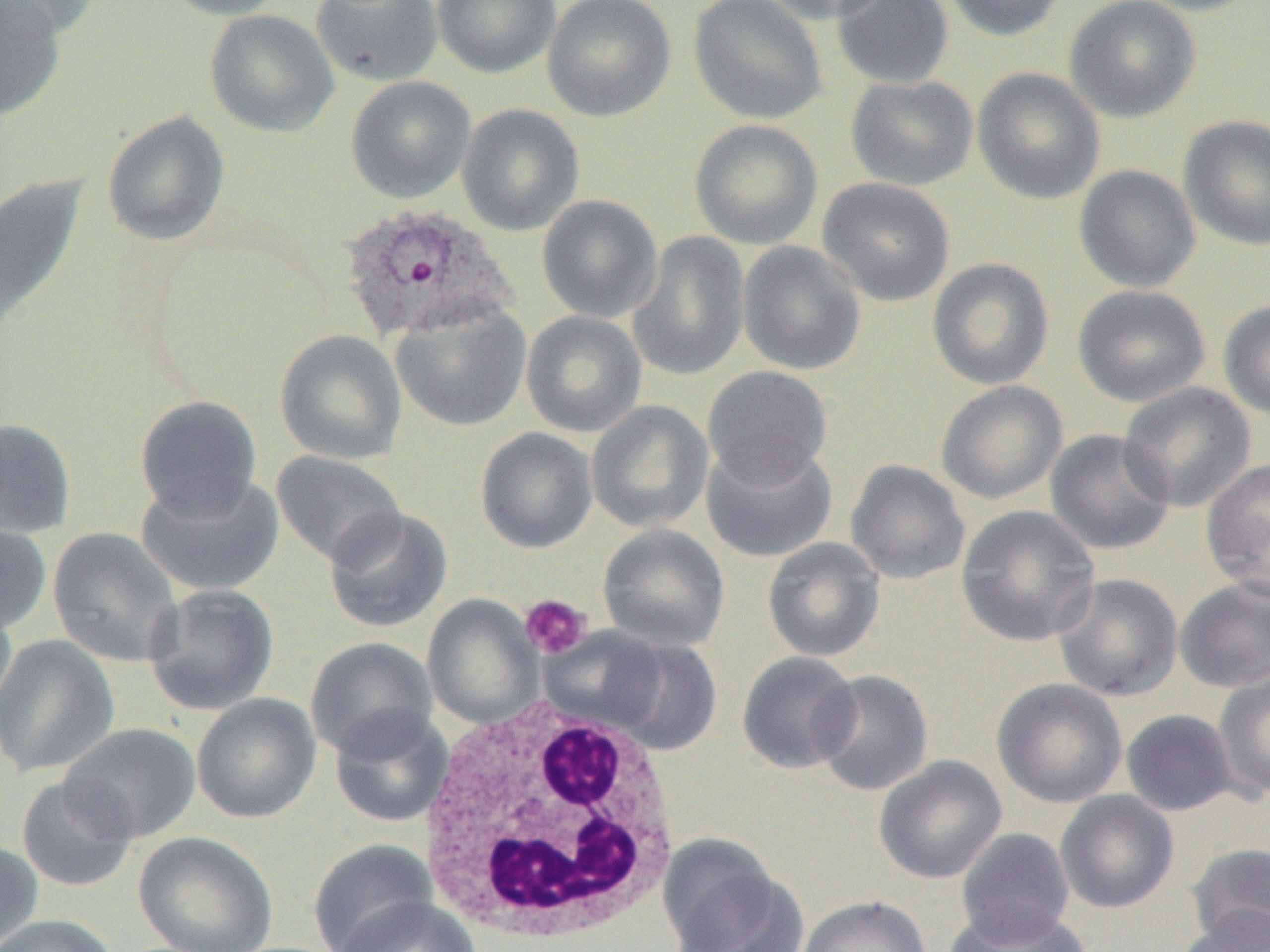

Approximate bounding boxes as [x1, y1, x2, y2] in pixels. White blood cell locations: [413, 698, 686, 945]. Plasmodium ovale-infected red blood cell locations: [339, 204, 516, 344]. Uninfected red blood cell locations: [0, 0, 103, 38], [0, 0, 66, 120], [156, 0, 293, 20], [311, 0, 444, 87], [431, 0, 561, 79], [542, 0, 676, 122], [688, 0, 829, 125], [759, 0, 895, 25], [832, 0, 954, 89], [939, 0, 1067, 41], [1064, 0, 1201, 123], [1130, 0, 1262, 16], [204, 9, 340, 137], [972, 67, 1106, 205], [345, 75, 476, 204], [845, 75, 978, 190], [456, 103, 585, 237], [101, 111, 231, 246], [1178, 114, 1270, 251], [689, 119, 823, 250], [1074, 164, 1202, 293], [0, 175, 88, 343], [817, 177, 956, 307], [536, 194, 663, 323], [627, 231, 750, 381], [737, 240, 867, 376], [927, 257, 1054, 390], [1072, 284, 1210, 407], [1218, 299, 1270, 420], [390, 301, 531, 432], [521, 311, 647, 438], [274, 330, 407, 465], [702, 366, 833, 487], [936, 380, 1068, 505], [1118, 382, 1257, 513], [134, 394, 263, 519], [586, 400, 714, 533], [0, 418, 77, 540], [474, 427, 598, 553], [1044, 429, 1176, 556], [701, 440, 838, 563], [270, 450, 407, 568], [1201, 457, 1270, 599], [845, 459, 970, 585], [136, 472, 284, 597], [956, 505, 1100, 647], [322, 506, 454, 635], [0, 520, 51, 635], [597, 524, 730, 652], [47, 528, 183, 667], [762, 537, 886, 662], [1052, 573, 1183, 702], [1174, 577, 1270, 693], [143, 584, 280, 716], [0, 593, 18, 720], [422, 594, 543, 728], [584, 631, 722, 756], [0, 634, 121, 777], [305, 637, 439, 760], [736, 651, 862, 774], [1214, 667, 1270, 800], [812, 669, 934, 796], [991, 678, 1127, 809], [191, 692, 322, 824], [328, 708, 453, 828], [1120, 708, 1240, 816], [59, 722, 202, 843], [874, 755, 1007, 884], [16, 775, 138, 892], [1055, 790, 1179, 913], [955, 827, 1075, 946], [133, 831, 278, 952], [0, 839, 43, 950], [307, 839, 438, 952], [658, 840, 802, 952], [1187, 842, 1270, 948], [796, 895, 931, 952], [336, 896, 483, 952], [945, 906, 1091, 952], [1179, 906, 1270, 952], [0, 914, 120, 952]. Platelet locations: [520, 594, 592, 660]. Slide-level diagnosis: Plasmodium ovale. Optical microscopy. Image is 1270×952 pixels. One field of a larger specimen. Thin blood smear. 1000x magnification.